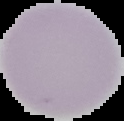

{
  "image_size": "124×121 pixels",
  "preparation": "thin blood film",
  "result": "no malaria parasites seen",
  "image_type": "segmented cell region on a black background"
}